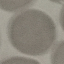
malaria status = uninfected
image type = cell patch, automatically extracted from a larger field of view and resized to 64 × 64 pixels
capture = smartphone camera at the microscope eyepiece
preparation = thin blood smear
stain = Giemsa